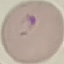

Result: malaria parasites detected. Automatically extracted cell patch, resized to 64 × 64 pixels. Thin blood film. Photographed with a smartphone camera at the microscope eyepiece. Giemsa stain.